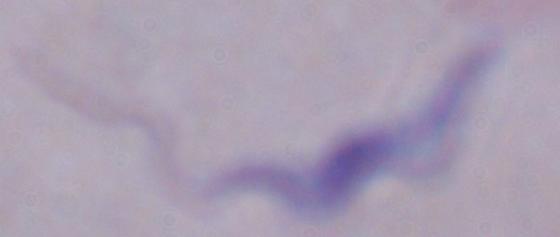
{
  "modality": "photomicrograph",
  "identification": "trypanosome",
  "magnification": "1000x"
}